Describe the morphology of the erythrocytes.
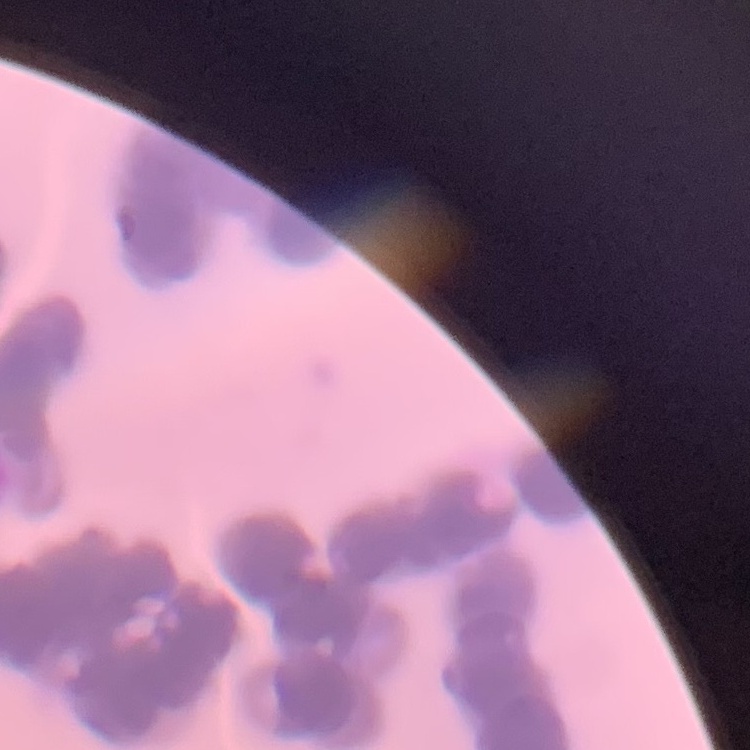
They show rouleaux formation.

Summary:
  - Preparation: thin blood smear
  - Stain: Field's or Giemsa
  - Image type: one tile cut from a larger photomicrograph